State which parasite is depicted.
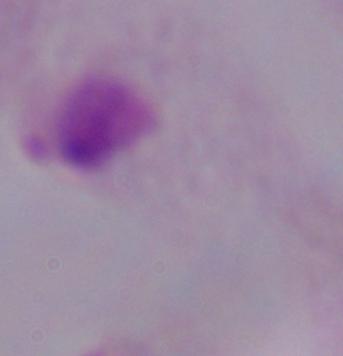
This is a trichomonad.

Summary:
  - Modality: photomicrograph
  - Magnification: 1000x